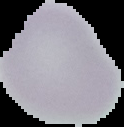

image_size: 124×127 pixels
image_type: segmented cell region on a black background
malaria_status: uninfected
preparation: thin blood smear